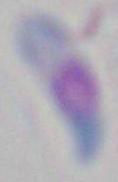

Summary:
  - Magnification: 1000x
  - Modality: photomicrograph
  - Identification: Toxoplasma gondii